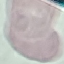
Summary:
  - Malaria status: uninfected
  - Capture: smartphone camera at the microscope eyepiece
  - Image type: automatically extracted cell patch, resized to 64 × 64 pixels
  - Stain: Giemsa
  - Preparation: thin blood smear